Assess this cell for malaria.
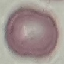

It is uninfected.

Summary:
  - Stain: Giemsa
  - Capture: smartphone through the microscope eyepiece
  - Image type: automatically extracted cell patch, resized to 64 × 64 pixels
  - Preparation: thin blood smear